Give the extent of all Plasmodium malariae-infected red blood cells.
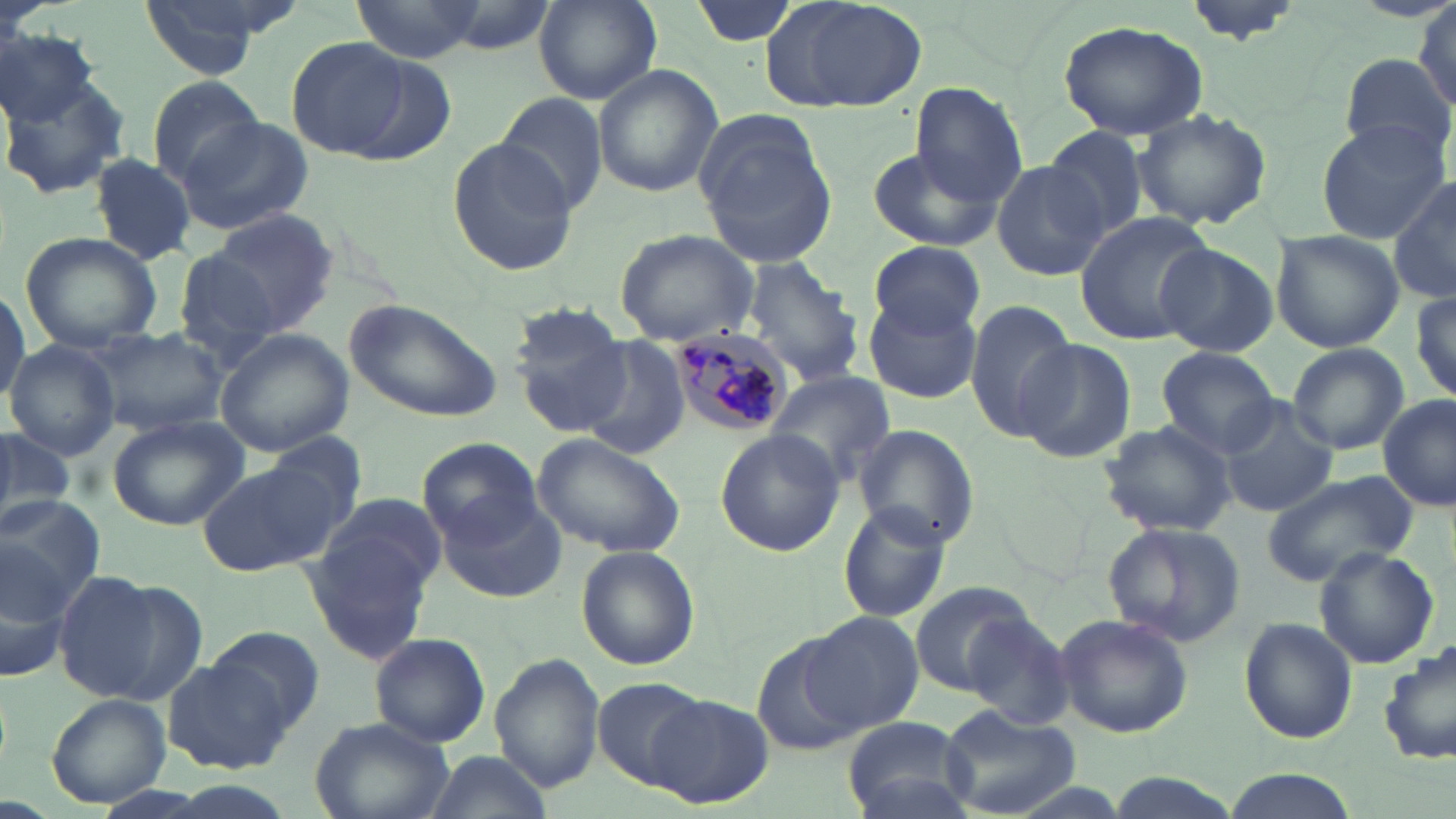
Approximate bounding boxes as [x1, y1, x2, y2] in pixels.
Plasmodium malariae-infected red blood cells: [662, 329, 788, 440].

Uninfected red blood cell locations: [138, 0, 290, 79], [351, 0, 480, 64], [687, 0, 801, 49], [760, 0, 927, 113], [535, 1, 660, 104], [1181, 1, 1307, 45], [1412, 6, 1456, 108], [1056, 18, 1210, 140], [0, 23, 96, 128], [286, 36, 414, 159], [1338, 50, 1451, 166], [592, 63, 723, 196], [1, 74, 133, 198], [147, 75, 267, 188], [910, 81, 1027, 205], [497, 91, 609, 216], [1131, 107, 1273, 231], [694, 113, 841, 269], [178, 117, 318, 235], [1314, 121, 1449, 244], [1043, 125, 1151, 242], [445, 135, 582, 276], [867, 146, 1000, 252], [89, 152, 200, 263], [990, 161, 1106, 281], [1388, 176, 1456, 307], [197, 210, 339, 339], [1073, 211, 1215, 348], [614, 228, 759, 348], [1270, 230, 1406, 353], [22, 234, 161, 349], [870, 240, 984, 336], [170, 241, 289, 362], [1157, 245, 1278, 357], [741, 256, 867, 387], [0, 284, 27, 404], [1409, 290, 1456, 408], [862, 293, 982, 405], [344, 296, 506, 424], [965, 299, 1078, 441], [510, 305, 644, 439], [88, 327, 232, 436], [215, 329, 355, 458], [577, 337, 692, 461], [1013, 338, 1136, 465], [4, 340, 118, 461], [1286, 342, 1409, 455], [1156, 347, 1281, 457], [763, 370, 894, 486], [1378, 397, 1455, 510], [1218, 399, 1339, 517], [107, 415, 245, 530], [1097, 419, 1238, 538], [853, 424, 979, 550], [713, 429, 844, 558], [0, 430, 77, 529], [534, 433, 684, 556], [419, 439, 544, 548], [198, 458, 345, 579], [1262, 469, 1420, 587], [303, 495, 446, 661], [0, 496, 105, 614], [440, 496, 565, 601], [838, 502, 953, 624], [1102, 522, 1247, 648], [576, 543, 701, 671], [1313, 546, 1438, 669], [0, 548, 77, 683], [50, 571, 167, 700], [909, 580, 1038, 695], [800, 610, 926, 735], [1053, 611, 1194, 739], [965, 612, 1077, 727], [1241, 618, 1357, 744], [207, 624, 326, 732], [368, 632, 490, 748], [753, 636, 867, 756], [1380, 642, 1456, 768], [491, 652, 605, 794], [164, 657, 292, 772], [592, 676, 707, 791], [647, 693, 773, 809], [45, 694, 172, 808], [938, 705, 1081, 818], [840, 714, 976, 818], [310, 719, 454, 819], [428, 752, 550, 817], [1220, 769, 1360, 819], [1106, 774, 1243, 819]. Slide-level diagnosis: Plasmodium malariae. Image is 1456×819 pixels. One field of a larger specimen. Light microscopy. 1000x magnification. Thin blood film. May-Grünwald-Giemsa-stained preparation.